Identify the blood parasite species.
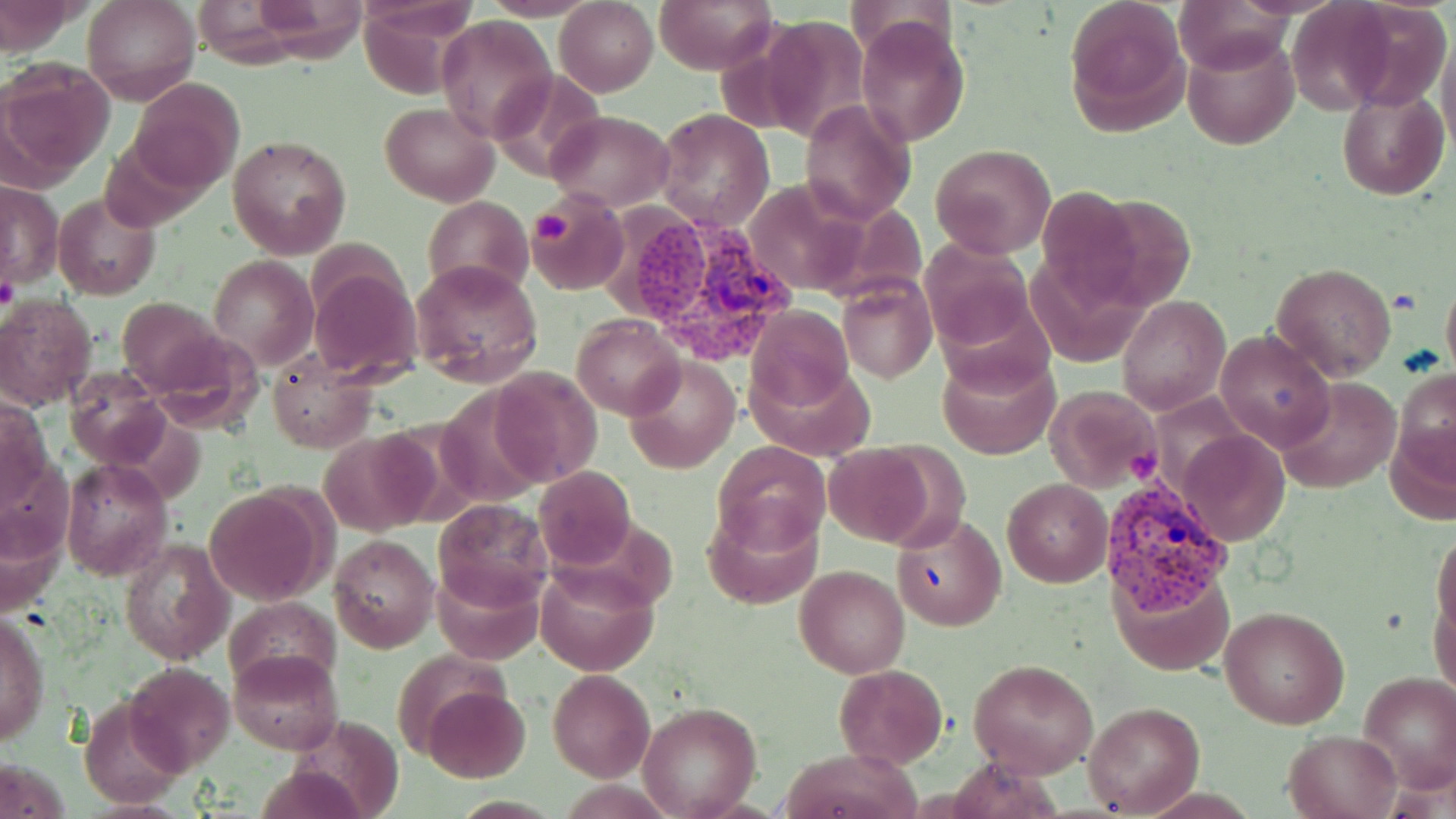
Plasmodium vivax.

Summary:
  - Coordinate format: approximate bounding boxes as [x1, y1, x2, y2] in pixels
  - Platelet locations: [531, 207, 571, 249], [1, 274, 19, 312]
  - Plasmodium vivax-infected red blood cell locations: [613, 207, 802, 372], [1101, 473, 1231, 610]
  - Uninfected red blood cell locations: [83, 0, 198, 106], [482, 0, 600, 20], [656, 0, 774, 74], [1065, 0, 1190, 130], [1336, 0, 1454, 114], [555, 1, 658, 96], [1174, 1, 1300, 72], [1284, 1, 1400, 114], [755, 14, 870, 142], [437, 16, 557, 140], [857, 19, 969, 146], [1435, 29, 1456, 153], [1182, 32, 1299, 151], [3, 66, 112, 184], [488, 70, 606, 182], [128, 78, 246, 193], [1337, 89, 1449, 199], [801, 99, 917, 225], [380, 103, 498, 205], [655, 109, 773, 229], [546, 111, 673, 210], [227, 133, 351, 260], [930, 143, 1056, 258], [741, 179, 872, 296], [1, 181, 62, 290], [53, 192, 161, 301], [525, 192, 629, 297], [422, 196, 533, 297], [918, 237, 1039, 355], [208, 255, 318, 371], [411, 258, 544, 388], [1270, 261, 1397, 379], [311, 264, 422, 384], [1441, 271, 1456, 383], [837, 273, 936, 384], [1117, 294, 1230, 416], [0, 297, 96, 409], [118, 297, 223, 395], [748, 305, 855, 412], [572, 315, 683, 418], [1217, 328, 1335, 452], [148, 333, 263, 433], [937, 351, 1059, 460], [266, 356, 375, 453], [625, 356, 740, 473], [487, 364, 603, 485], [1393, 367, 1456, 486], [66, 369, 171, 469], [1274, 377, 1399, 493], [1044, 385, 1162, 491], [1, 395, 50, 508], [319, 429, 440, 537], [1177, 430, 1290, 546], [712, 439, 832, 557], [821, 444, 940, 548], [60, 460, 173, 581], [534, 467, 637, 571], [1002, 478, 1112, 586], [205, 486, 330, 604], [705, 500, 822, 611], [434, 502, 551, 611], [891, 512, 1004, 630], [1432, 526, 1456, 642], [330, 534, 438, 653], [116, 537, 233, 665], [433, 559, 543, 666], [536, 561, 657, 676], [795, 565, 908, 678], [1109, 565, 1234, 676], [1430, 582, 1454, 705], [222, 597, 341, 692], [1219, 605, 1350, 731], [0, 611, 49, 749], [231, 648, 343, 753], [969, 658, 1098, 776], [125, 662, 235, 775], [832, 663, 948, 769], [548, 669, 656, 781], [1358, 673, 1456, 793], [424, 686, 529, 783], [79, 697, 186, 806], [1082, 701, 1205, 816], [638, 702, 762, 817], [287, 713, 403, 819], [1282, 730, 1403, 819], [781, 748, 919, 819]
  - Image size: 1456×819 pixels
  - Modality: light microscopy
  - Magnification: 1000x
  - Preparation: thin blood smear
  - Stain: May-Grünwald-Giemsa
  - Field of view: one of a larger specimen